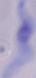

identification = trypanosome
modality = micrograph
magnification = 1000x